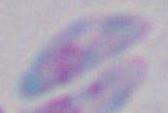
{
  "magnification": "1000x",
  "identification": "Toxoplasma gondii",
  "modality": "micrograph"
}